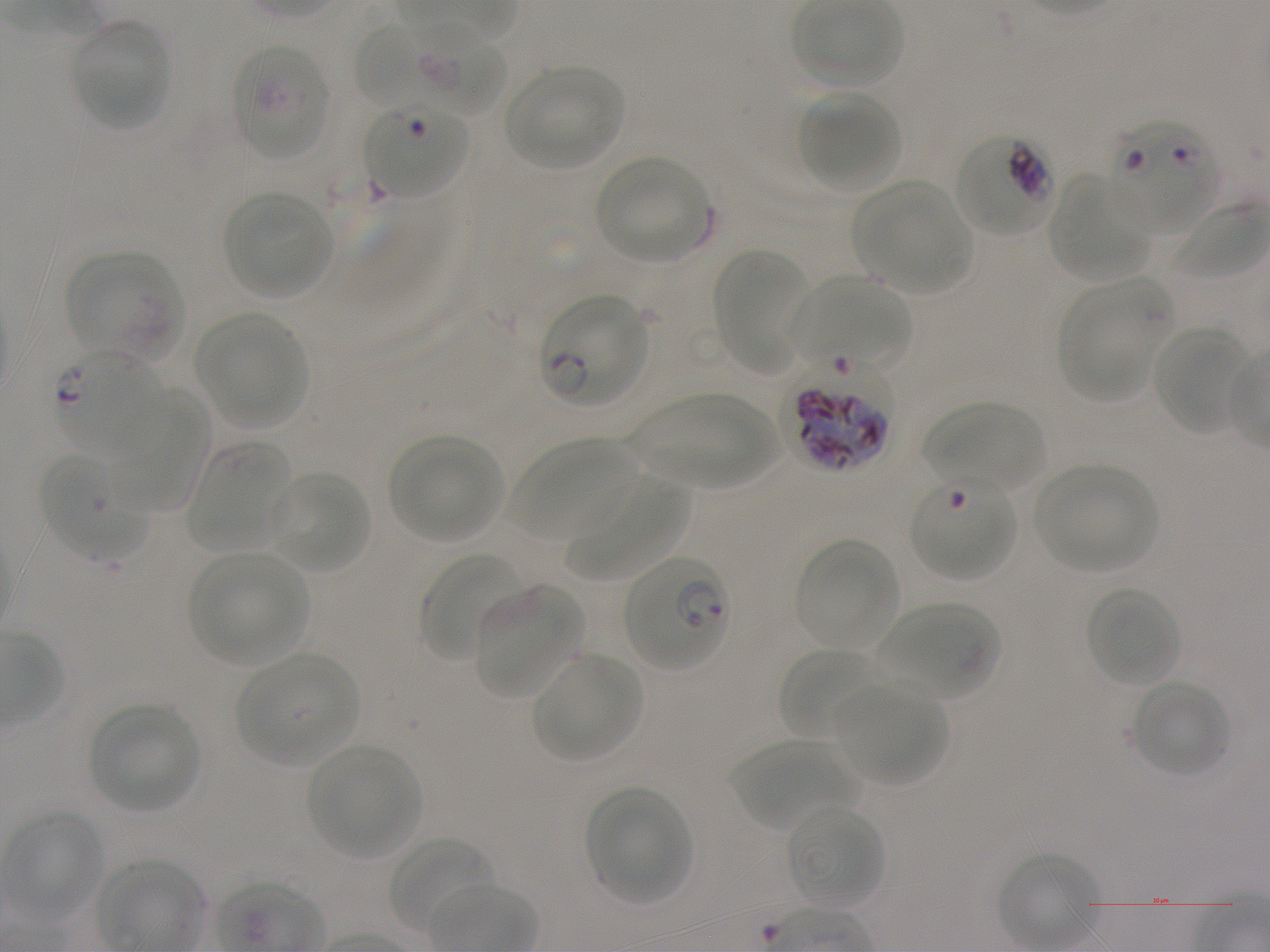

Approximate bounding boxes as (x1, y1, x2, y2) in pixels. Not every red blood cell is marked. A life-cycle stage — or a range of stages, where the recorded stages span more than one — follows each staged infected red blood cell.
Summary:
  - Locations of infected red blood cells: (1109, 117, 1219, 236); (956, 134, 1055, 237) trophozoite; (539, 294, 651, 407) ring; (53, 348, 164, 456) ring; (621, 554, 729, 671) ring
  - Locations of red blood cells of indeterminate infection status: (393, 22, 514, 119), (230, 42, 330, 161), (363, 102, 467, 200), (64, 247, 184, 361), (791, 276, 911, 373), (789, 380, 891, 488), (910, 477, 1016, 581)
  - Locations of uninfected red blood cells: (69, 19, 173, 130), (358, 25, 416, 105), (505, 65, 626, 170), (799, 94, 900, 189), (592, 155, 712, 262), (1050, 176, 1149, 281), (855, 181, 972, 293), (221, 191, 336, 299), (712, 248, 808, 368), (1059, 278, 1168, 403), (195, 313, 307, 426), (1152, 326, 1250, 434), (111, 390, 211, 517), (636, 393, 778, 488), (923, 401, 1046, 493), (390, 435, 503, 541), (511, 439, 633, 539), (190, 442, 295, 554), (42, 453, 146, 561), (1034, 464, 1157, 574), (272, 470, 370, 574), (567, 476, 692, 581), (794, 536, 900, 650), (421, 551, 523, 660), (189, 553, 310, 666), (472, 583, 582, 696), (1085, 586, 1182, 688), (882, 602, 999, 700), (779, 647, 879, 739), (235, 652, 359, 766), (532, 653, 644, 762), (1130, 679, 1231, 778), (832, 681, 949, 786), (88, 703, 200, 812), (729, 739, 852, 832), (306, 744, 422, 858), (585, 787, 692, 903), (786, 804, 885, 908), (387, 835, 491, 935)
  - Life-cycle stages observed: ring, trophozoite
  - Field of view: one from this slide
  - Image size: 1270×952 pixels
  - Donor blood group: A+
  - Objective: 100x, oil immersion, numerical aperture 1.25
  - Stain: Giemsa
  - Preparation: thin blood smear
  - Culture: in-vitro Plasmodium falciparum strain NF54, static